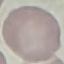
Summary:
  - Malaria status: uninfected
  - Image type: cell patch, automatically extracted from a larger field of view and resized to 64 × 64 pixels
  - Stain: Giemsa
  - Capture: smartphone through the microscope eyepiece
  - Preparation: thin blood smear